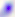
Toxoplasma gondii is seen. Micrograph. 400x magnification.